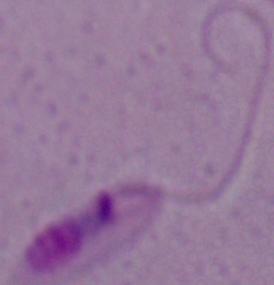 A Leishmania parasite is seen. Micrograph. Captured at 1000x magnification.